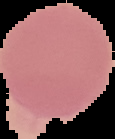 Image is 115×139 pixels. The area outside the segmented cell region is set to black. Malaria status: uninfected. From a thin blood smear.